Classify this cell by malaria status.
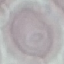
It is uninfected.

Acquired by smartphone through the microscope eyepiece. Thin blood film. Cell patch, automatically extracted from a larger field of view and resized to 64 × 64 pixels. Giemsa stain.